Give the extent of all uninfected red blood cells.
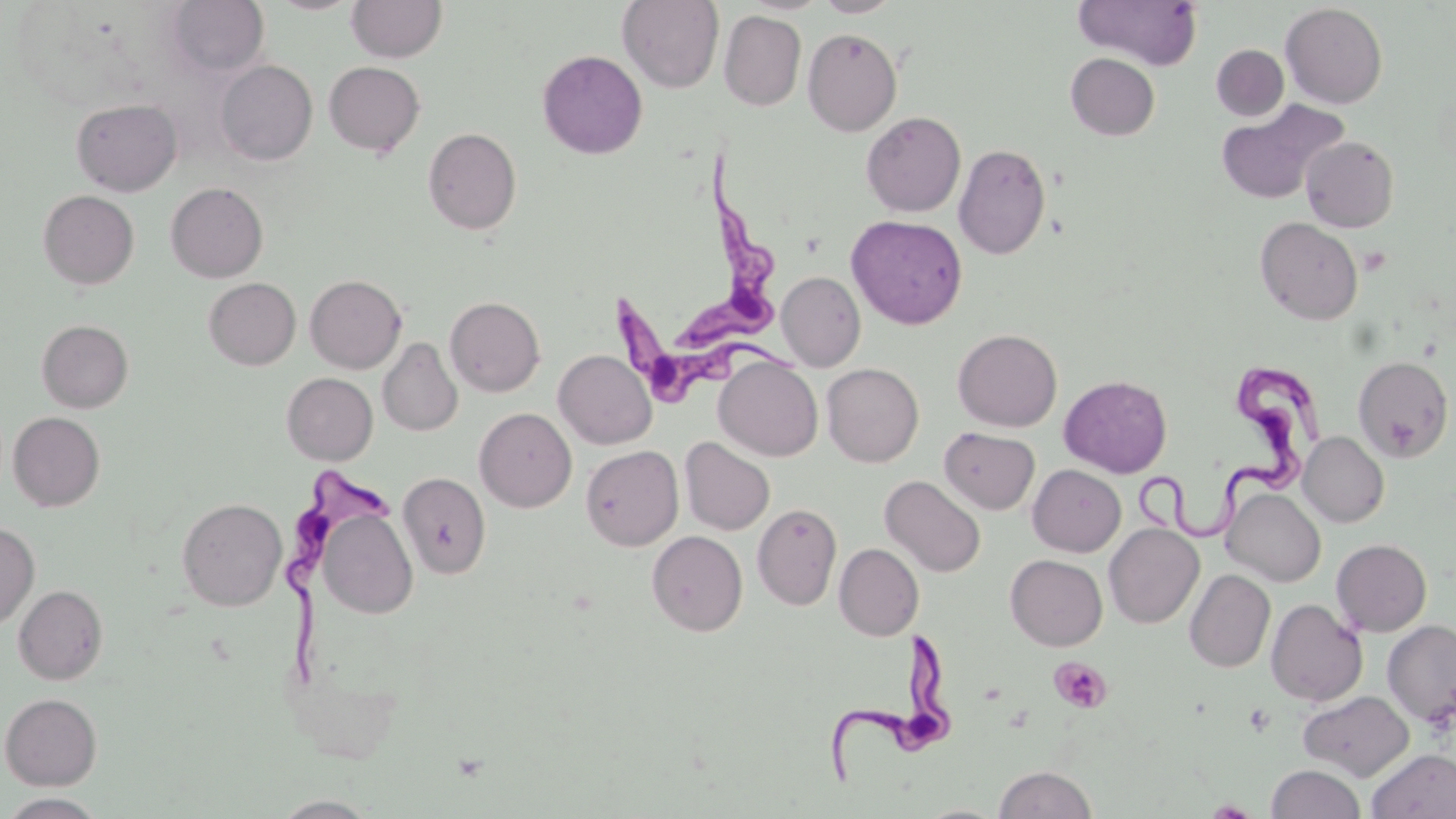

Approximate bounding boxes as [x1, y1, x2, y2] in pixels.
Uninfected red blood cells: [165, 0, 269, 77], [267, 0, 365, 15], [618, 0, 724, 93], [813, 0, 903, 17], [1073, 0, 1203, 69], [347, 1, 447, 62], [1280, 3, 1388, 108], [719, 11, 807, 110], [802, 28, 902, 136], [1211, 45, 1289, 121], [537, 49, 648, 160], [1066, 53, 1160, 140], [216, 60, 317, 165], [323, 61, 425, 156], [71, 98, 182, 195], [1215, 100, 1347, 205], [861, 111, 966, 217], [423, 127, 522, 235], [1302, 136, 1399, 232], [954, 143, 1050, 260], [165, 182, 268, 282], [38, 190, 139, 289], [846, 214, 967, 329], [1255, 217, 1363, 325], [777, 272, 866, 371], [305, 274, 407, 373], [203, 277, 300, 370], [445, 296, 545, 397], [36, 319, 133, 412], [953, 328, 1062, 432], [378, 337, 463, 436], [553, 349, 657, 449], [714, 356, 823, 461], [1353, 356, 1454, 462], [822, 363, 924, 467], [282, 372, 378, 465], [1059, 375, 1172, 478], [474, 407, 576, 512], [8, 412, 105, 511], [939, 427, 1039, 515], [1299, 431, 1389, 527], [680, 437, 775, 535], [581, 445, 683, 550], [1028, 464, 1126, 556], [398, 472, 491, 578], [880, 475, 986, 577], [1222, 487, 1326, 586], [177, 497, 287, 611], [752, 503, 842, 610], [318, 509, 417, 619], [0, 520, 39, 629], [1104, 523, 1204, 628], [647, 530, 748, 636], [1331, 539, 1432, 636], [834, 543, 923, 640], [1005, 554, 1107, 650], [1184, 569, 1275, 672], [14, 584, 108, 684], [1266, 598, 1367, 707], [1382, 619, 1456, 726], [1298, 690, 1414, 780], [1, 693, 101, 790], [1367, 749, 1456, 819], [1267, 764, 1366, 819], [993, 765, 1099, 818], [0, 793, 109, 818], [270, 795, 380, 818].

slide_level_diagnosis: Trypanosoma brucei
magnification: 1000x
platelet_locations: 'approximate bounding boxes as [x1, y1, x2, y2] in pixels: [1049, 657, 1112, 714], [1243, 702, 1274, 736]'
image_size: 1456×819 pixels
field_of_view: one of a larger specimen
stain: May-Grünwald-Giemsa
preparation: thin blood film
modality: light microscopy
trypanosoma_brucei_locations: 'approximate bounding boxes as [x1, y1, x2, y2] in pixels: [673, 163, 790, 348], [606, 289, 799, 392], [1136, 369, 1334, 538], [286, 464, 401, 688], [823, 627, 959, 784]'